Give the position of every malaria parasite.
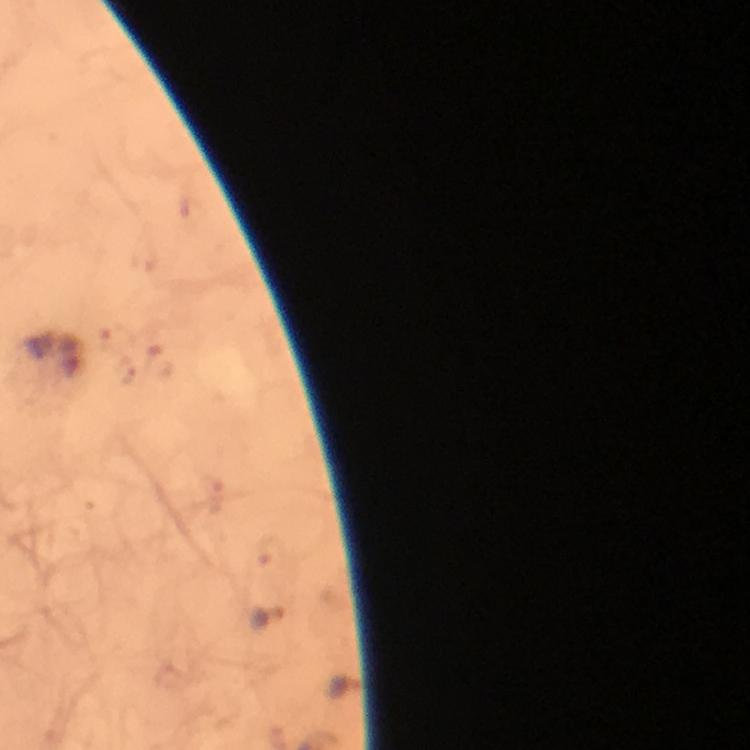
Approximate object centers, in pixels from the top-left corner.
Malaria parasites: (x=109, y=336), (x=161, y=361), (x=124, y=372), (x=267, y=617), (x=342, y=685).

Summary:
  - Capture: smartphone photograph through a microscope
  - Cropped from: one field of view
  - Preparation: thick blood smear
  - Context: from a malaria diagnostic workup
  - Magnification: 100x
  - Stain: Giemsa
  - Immersion oil: applied
  - Image size: 750×750 pixels